Report the malaria status of this cell.
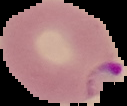

It is parasitized.

Segmented cell region on a black background. From a thin blood smear. Image is 127×106 pixels.